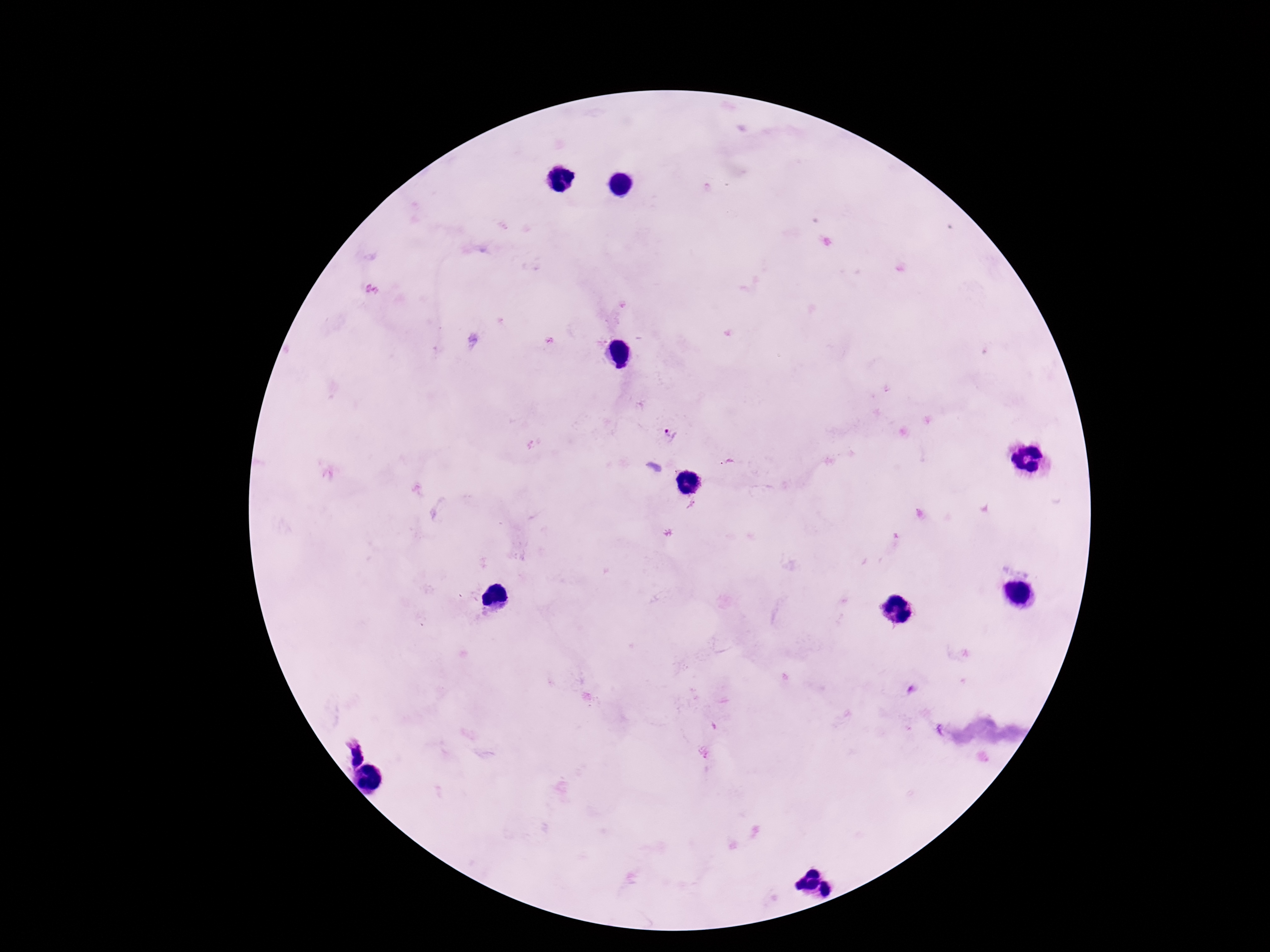

Approximate centers as (x, y) in pixels. Plasmodium parasite locations: (671, 435), (354, 752). Single field of view. Thick blood smear. Patient malaria status: positive. Smartphone photograph taken through the microscope eyepiece. Giemsa-stained preparation. 100x magnification. Image is 1270×952 pixels.